Give the extent of all Plasmodium malariae-infected red blood cells.
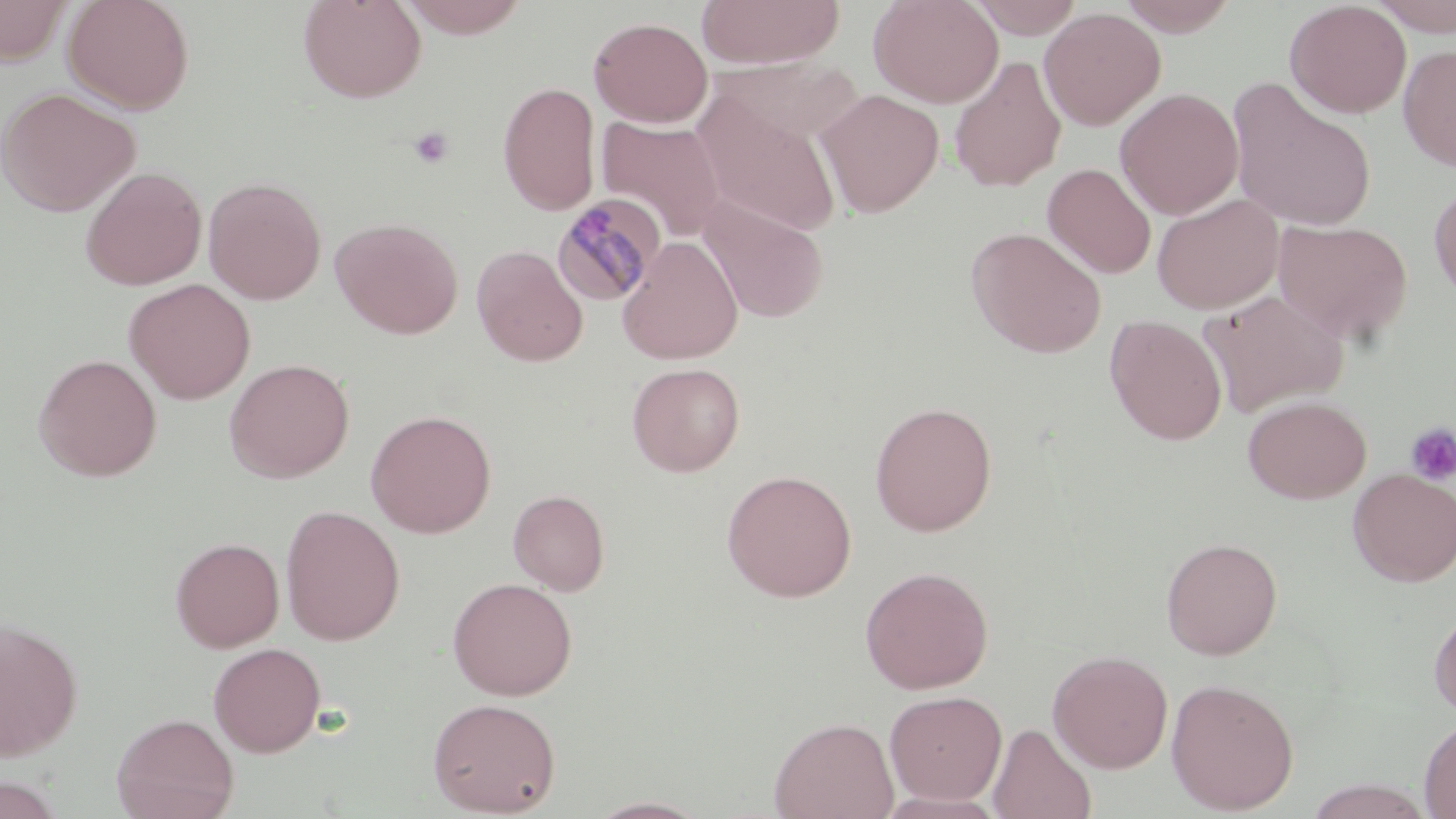
Approximate bounding boxes as (x1, y1, x2, y2) in pixels.
Plasmodium malariae-infected red blood cells: (552, 194, 666, 307).

Summary:
  - Platelet locations: (408, 126, 455, 169), (1404, 422, 1456, 486)
  - Uninfected red blood cell locations: (0, 0, 75, 65), (63, 0, 195, 114), (298, 0, 427, 103), (396, 0, 533, 38), (696, 0, 843, 69), (868, 0, 1004, 108), (968, 0, 1084, 39), (1117, 0, 1241, 37), (1284, 0, 1411, 118), (1367, 0, 1456, 37), (1039, 7, 1166, 131), (588, 16, 713, 127), (1398, 44, 1456, 172), (949, 56, 1066, 193), (710, 57, 860, 148), (1226, 79, 1378, 233), (497, 81, 601, 216), (1, 87, 140, 217), (1114, 87, 1244, 220), (691, 89, 844, 238), (816, 89, 944, 218), (596, 115, 727, 241), (1042, 163, 1157, 279), (80, 166, 206, 290), (203, 176, 326, 305), (1429, 181, 1456, 307), (1152, 193, 1284, 314), (697, 196, 828, 323), (331, 216, 464, 339), (1273, 218, 1413, 345), (967, 227, 1107, 358), (618, 235, 743, 365), (472, 245, 588, 366), (123, 278, 256, 404), (1200, 289, 1348, 417), (1105, 315, 1227, 446), (33, 354, 162, 482), (224, 358, 354, 482), (626, 362, 745, 476), (1242, 395, 1372, 504), (869, 401, 997, 536), (365, 409, 496, 538), (1348, 468, 1456, 586), (721, 469, 857, 602), (508, 489, 610, 595), (280, 505, 405, 645), (170, 536, 285, 652), (1160, 536, 1283, 660), (859, 565, 994, 694), (447, 577, 577, 700), (1428, 603, 1456, 718), (0, 618, 83, 761), (208, 642, 325, 757), (1048, 649, 1173, 773), (1165, 677, 1299, 814), (885, 690, 1007, 805), (426, 696, 561, 817), (111, 712, 239, 819), (769, 716, 899, 819), (1419, 717, 1456, 818), (988, 721, 1096, 819), (0, 774, 67, 819), (1302, 778, 1437, 819), (586, 795, 712, 818)
  - Slide-level diagnosis: Plasmodium malariae
  - Preparation: thin blood smear
  - Field of view: one of a larger specimen
  - Magnification: 1000x
  - Stain: May-Grünwald-Giemsa
  - Modality: light microscopy
  - Image size: 1456×819 pixels